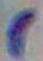 Photomicrograph. 1000x magnification. Toxoplasma gondii is seen.